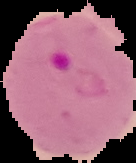
image_type: cell region segmented out of the field of view; surrounding area masked to black
preparation: thin blood film
image_size: 136×163 pixels
result: Plasmodium parasites detected